Name the blood parasite species.
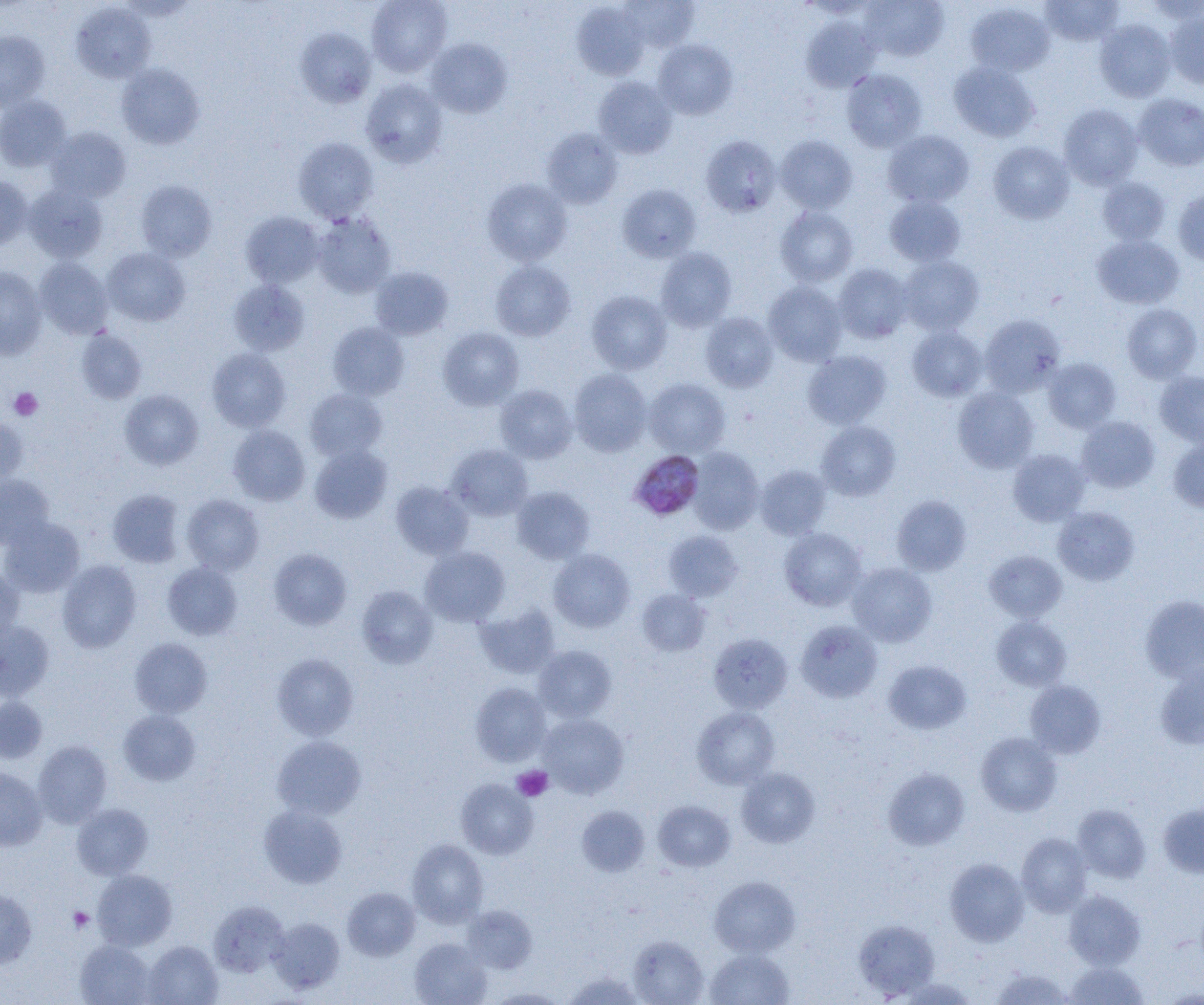

Plasmodium malariae.

Summary:
  - Coordinate format: approximate bounding boxes as (x1,y1)-(x2,y2) corner pairs in pixels
  - Plasmodium malariae-infected red blood cell locations: (628,449)-(705,521)
  - Uninfected red blood cell locations: (367,0)-(452,76), (620,0)-(699,51), (859,0)-(949,61), (1040,0)-(1124,46), (572,2)-(649,80), (70,3)-(155,83), (965,3)-(1055,76), (1166,8)-(1204,88), (801,17)-(881,92), (1094,19)-(1176,102), (295,27)-(376,108), (0,30)-(50,111), (426,38)-(512,118), (653,39)-(737,119), (948,61)-(1040,142), (116,63)-(205,149), (841,68)-(927,153), (592,76)-(677,159), (361,78)-(448,168), (1133,93)-(1204,171), (0,95)-(71,172), (1059,104)-(1143,189), (46,127)-(130,202), (541,128)-(623,209), (883,130)-(974,208), (701,135)-(782,218), (776,135)-(857,213), (293,137)-(379,222), (988,141)-(1074,223), (0,175)-(33,250), (1097,177)-(1171,245), (482,179)-(572,266), (136,180)-(216,261), (23,184)-(108,262), (618,184)-(701,263), (1173,188)-(1204,266), (884,195)-(966,267), (775,206)-(858,287), (241,211)-(324,288), (312,213)-(396,298), (1092,235)-(1184,309), (103,247)-(190,326), (656,248)-(737,331), (898,255)-(984,335), (34,257)-(113,339), (490,260)-(576,341), (834,263)-(913,343), (0,266)-(48,360), (370,266)-(454,340), (228,279)-(309,356), (763,281)-(847,366), (587,290)-(672,374), (1122,304)-(1201,382), (700,312)-(778,392), (979,314)-(1065,397), (327,322)-(410,400), (907,326)-(987,401), (438,327)-(524,410), (76,329)-(147,404), (207,347)-(291,432), (803,350)-(891,429), (1043,358)-(1121,433), (568,368)-(652,457), (1155,371)-(1204,446), (644,378)-(730,457), (494,384)-(577,463), (952,387)-(1039,473), (304,388)-(387,462), (119,390)-(203,470), (0,416)-(28,485), (1077,416)-(1160,492), (816,421)-(901,501), (228,425)-(310,505), (1167,438)-(1204,512), (309,444)-(392,523), (447,444)-(532,520), (687,447)-(764,534), (1008,449)-(1090,526), (755,464)-(831,539), (0,474)-(54,549), (390,481)-(473,559), (512,486)-(595,564), (108,489)-(184,567), (182,494)-(264,575), (891,495)-(971,576), (1053,506)-(1139,585), (0,517)-(85,598), (779,527)-(867,611), (664,530)-(743,602), (420,546)-(510,626), (268,548)-(352,630), (548,549)-(635,633), (983,550)-(1067,622), (57,559)-(142,653), (163,562)-(243,640), (847,563)-(937,646), (0,567)-(24,649), (357,585)-(438,669), (637,589)-(711,656), (1140,595)-(1204,682), (474,604)-(560,679), (992,615)-(1071,690), (796,620)-(882,703), (0,622)-(54,701), (708,633)-(792,714), (129,638)-(213,718), (533,645)-(617,723), (272,653)-(359,740), (884,660)-(971,734), (1155,662)-(1204,750), (1024,680)-(1106,758), (470,682)-(551,767), (0,696)-(47,763), (691,706)-(780,789), (118,710)-(200,785), (538,713)-(629,798), (976,732)-(1061,816), (272,735)-(366,820), (33,740)-(112,827), (0,767)-(47,851), (737,767)-(819,847), (883,768)-(969,850), (456,779)-(538,859), (653,800)-(735,871), (1158,801)-(1204,878), (72,803)-(153,880), (258,804)-(348,888), (1072,804)-(1151,882), (576,805)-(650,876), (1016,832)-(1092,916), (407,839)-(488,927), (945,858)-(1029,946), (92,869)-(177,950), (709,876)-(800,957), (342,887)-(420,961), (0,888)-(36,969), (1063,890)-(1145,970), (208,900)-(289,977), (462,905)-(537,974), (269,918)-(345,993), (853,918)-(940,999), (627,935)-(708,1005), (409,938)-(491,1005), (75,940)-(155,1005), (143,940)-(222,1005), (705,949)-(794,1005), (1065,961)-(1149,1004), (990,968)-(1075,1004), (563,972)-(646,1005), (897,977)-(978,1005), (487,988)-(569,1004)
  - Platelet locations: (9,388)-(43,421), (512,765)-(553,801), (68,907)-(94,933)
  - Magnification: 1000x
  - Preparation: thin blood film
  - Modality: optical microscopy
  - Image size: 1204×1005 pixels
  - Field of view: one of a larger specimen